State which parasite is depicted.
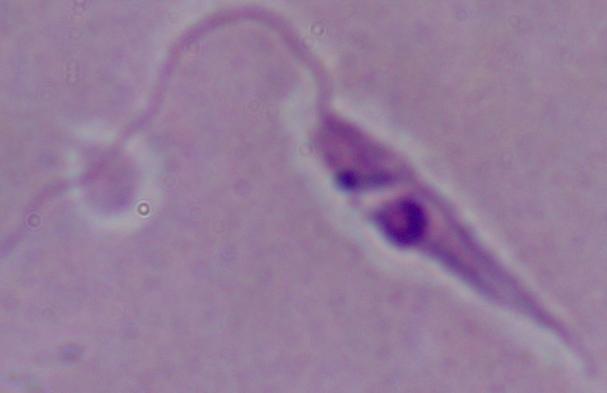
Leishmania.

Summary:
  - Modality: micrograph
  - Magnification: 1000x